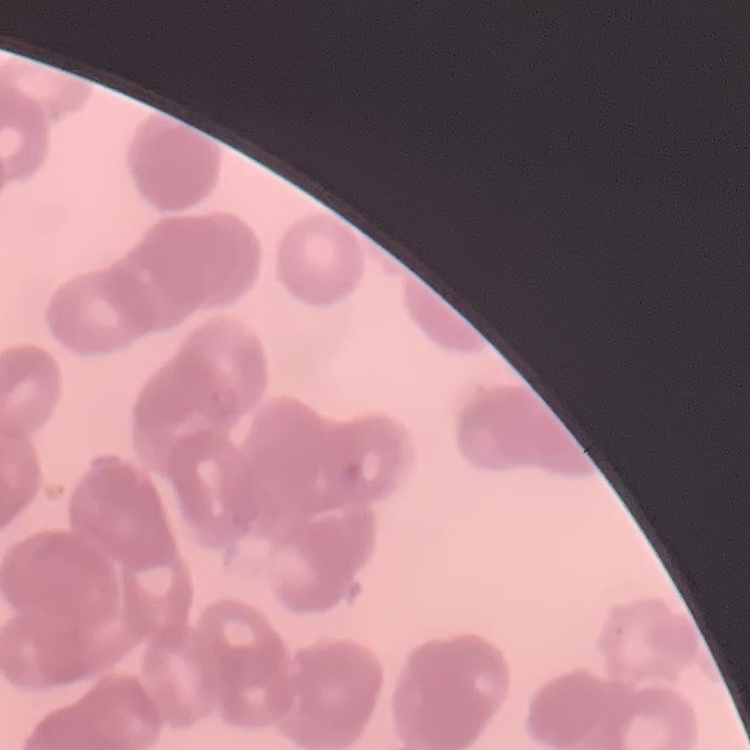

Summary:
  - Red blood cell morphology: rouleaux formation
  - Image type: square crop of a larger photomicrograph
  - Preparation: thin blood film
  - Stain: Field's or Giemsa